Classify this cell by malaria status.
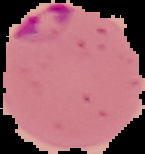

It is parasitized.

image type = cell region segmented out of the field of view; surrounding area masked to black
preparation = thin blood smear
image size = 145×154 pixels